Describe the morphology of the red blood cells.
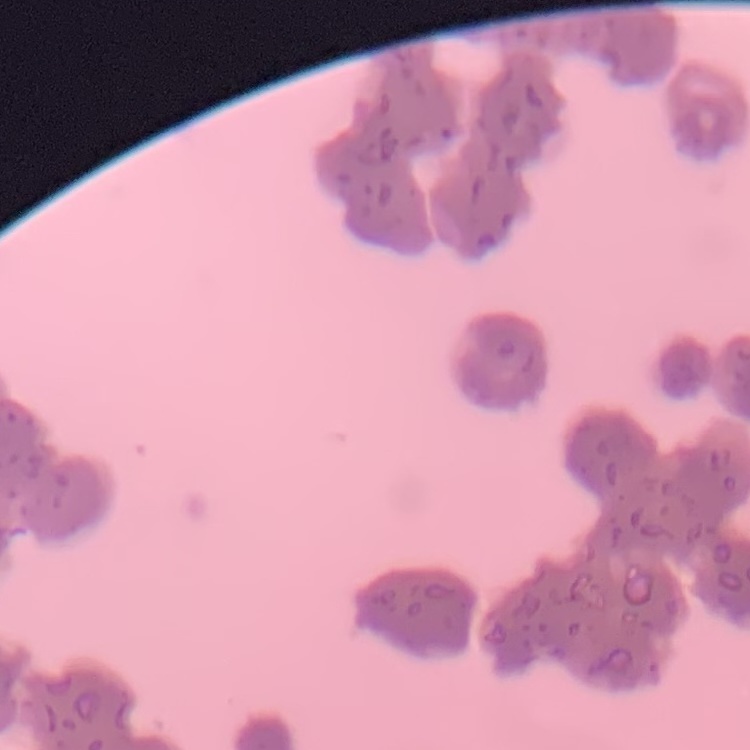
Rouleaux formation.

stain = Field's or Giemsa
preparation = thin peripheral smear
image type = one tile cut from a larger photomicrograph